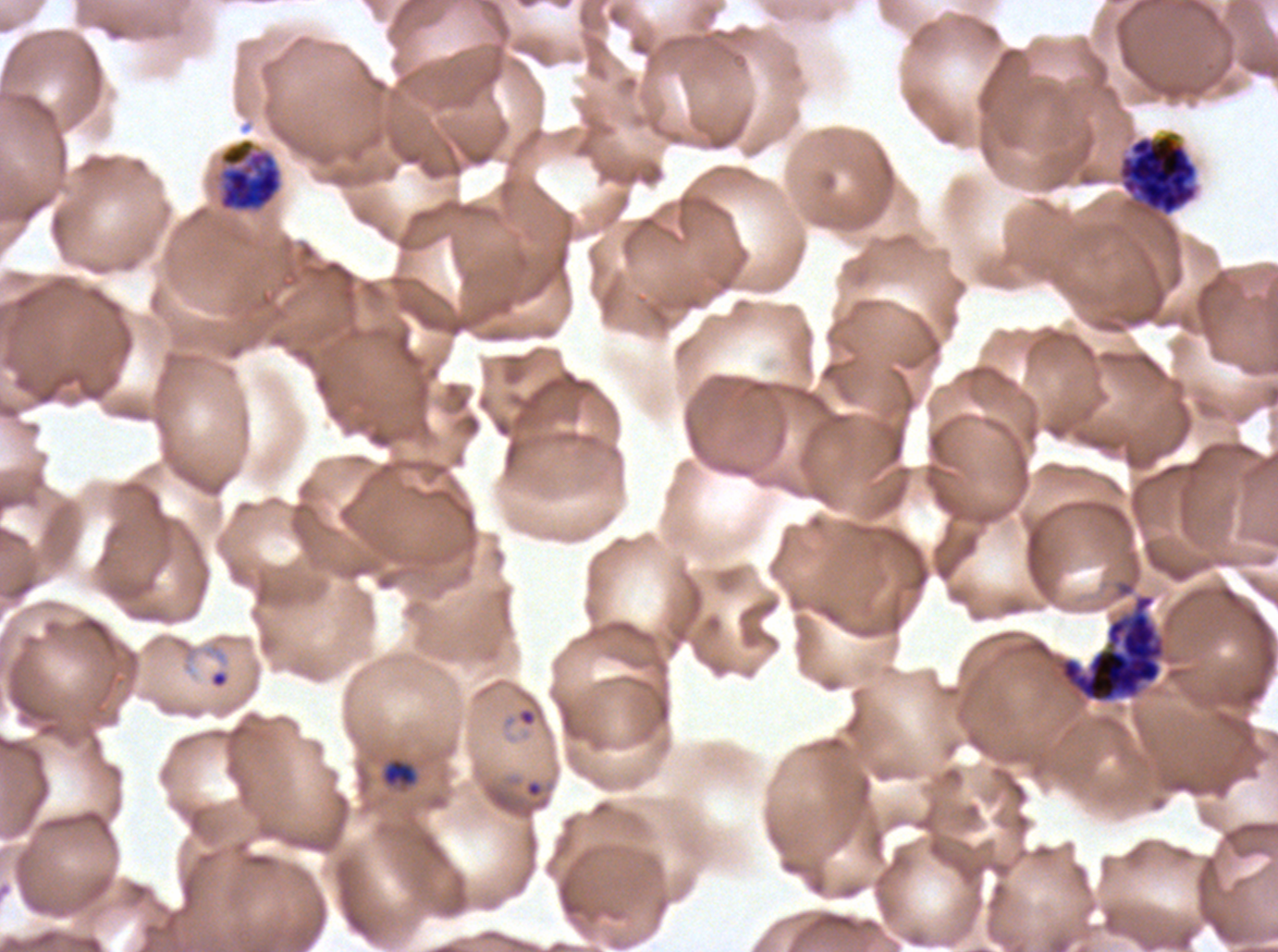 Approximate bounding boxes as (x1, y1, x2, y2) in pixels. Ring locations: (209, 669, 229, 689), (517, 707, 537, 727), (524, 780, 544, 799). Early schizont locations: (218, 139, 282, 212). Late schizont locations: (1117, 131, 1198, 216), (1060, 593, 1165, 702). Late-ring/early-trophozoite locations: (382, 759, 417, 787). Image is 1278×952 pixels. One sub-image of a larger composite. P. falciparum cultured ex vivo for 24 to 48 hours, from a patient in The Gambia. Thin blood smear. Life-cycle stages observed: ring, late-ring/early-trophozoite, early schizont, late schizont. Giemsa-stained preparation.